Assess the morphology of the red blood cells.
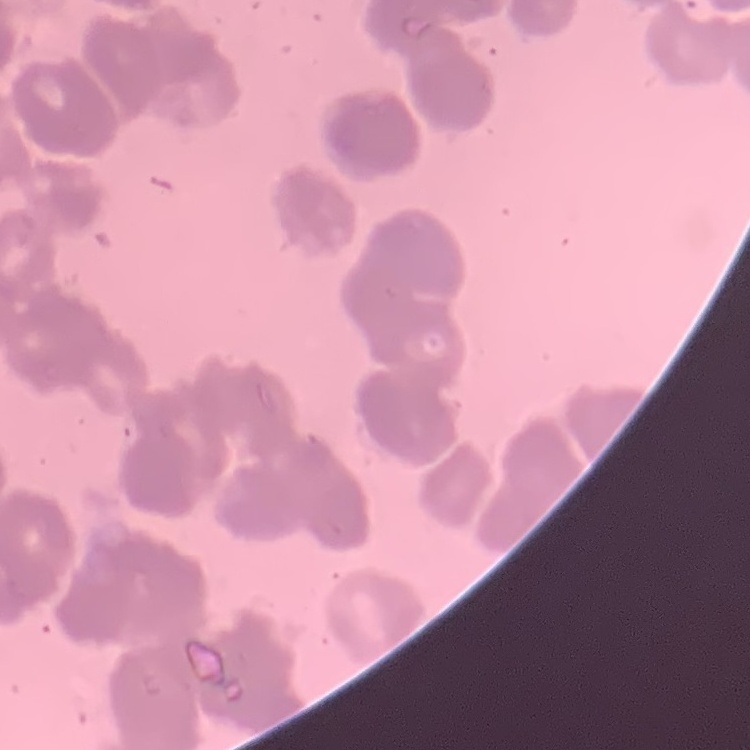
Rouleaux formation.

stain = Field's or Giemsa
image type = square crop of a larger photomicrograph
preparation = thin blood film